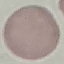
Malaria status: uninfected. Acquired by smartphone through the microscope eyepiece. Automatically extracted cell patch, resized to 64 × 64 pixels. Thin smear of blood. Giemsa stain.